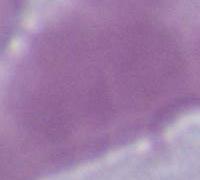
modality = photomicrograph
magnification = 1000x
identification = red blood cell